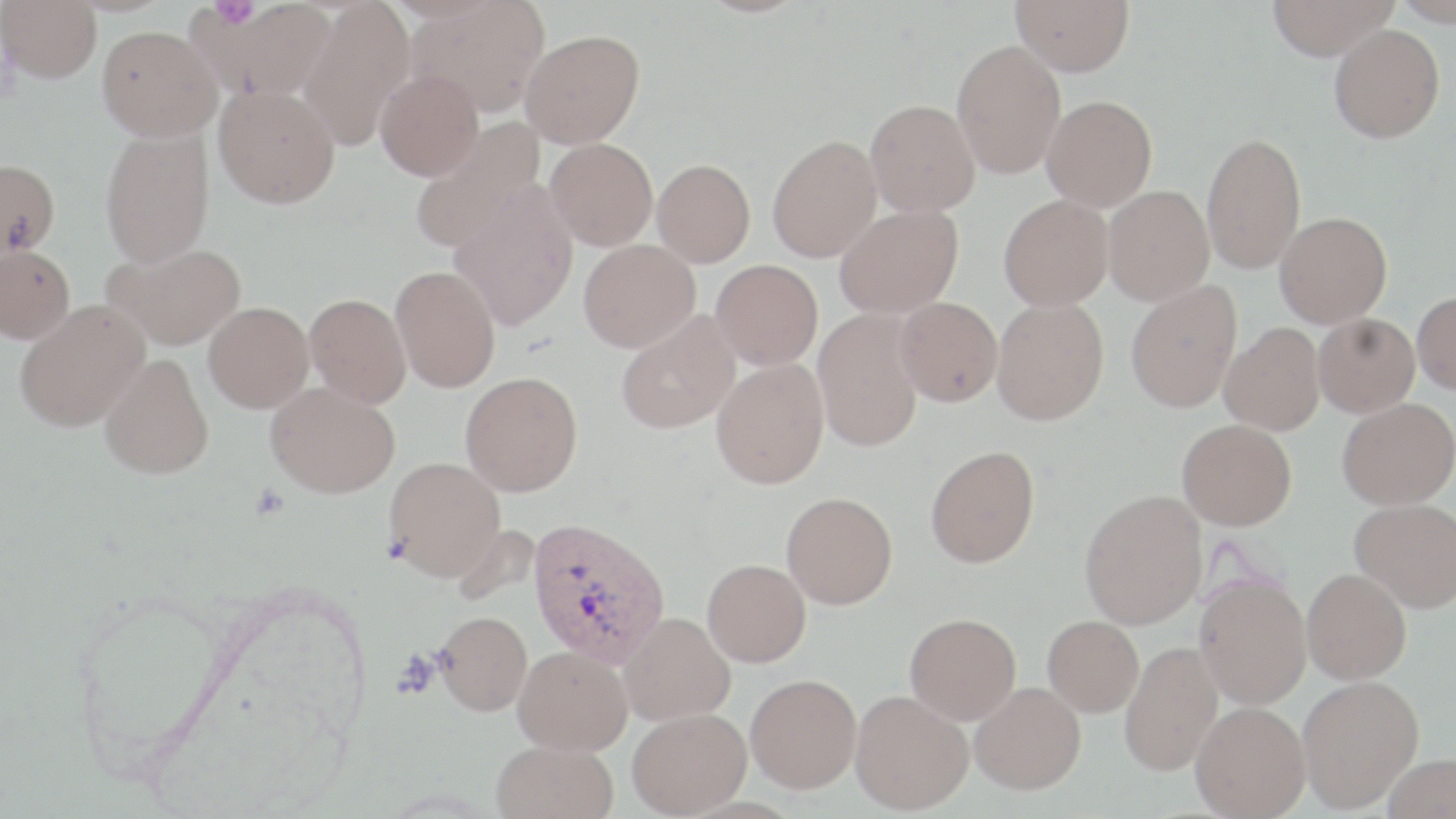
{
  "slide_level_diagnosis": "Plasmodium vivax",
  "image_size": "1456×819 pixels",
  "stain": "May-Grünwald-Giemsa",
  "modality": "optical microscopy",
  "uninfected_red_blood_cell_locations": "approximate bounding boxes as [x1, y1, x2, y2] in pixels: [1, 0, 101, 82], [200, 0, 336, 99], [407, 0, 551, 117], [1010, 0, 1134, 76], [1265, 0, 1399, 60], [1392, 0, 1456, 26], [299, 1, 417, 151], [1329, 23, 1445, 143], [97, 25, 222, 140], [520, 29, 644, 148], [952, 40, 1066, 179], [374, 69, 484, 181], [214, 85, 339, 208], [1042, 95, 1157, 211], [865, 99, 980, 216], [407, 119, 545, 253], [99, 127, 214, 268], [1201, 131, 1306, 274], [767, 134, 882, 262], [545, 138, 658, 251], [0, 159, 60, 258], [652, 159, 756, 266], [449, 184, 579, 330], [1103, 185, 1214, 305], [998, 194, 1113, 311], [834, 205, 963, 318], [1275, 211, 1392, 327], [578, 240, 700, 352], [103, 242, 247, 350], [0, 244, 75, 343], [711, 259, 823, 370], [390, 265, 501, 393], [1125, 280, 1242, 412], [1412, 292, 1456, 394], [304, 293, 412, 408], [991, 295, 1109, 425], [895, 297, 1003, 406], [14, 300, 149, 431], [204, 302, 314, 413], [812, 309, 924, 452], [616, 312, 740, 434], [1314, 312, 1420, 416], [1219, 323, 1325, 435], [100, 353, 214, 479], [711, 358, 829, 489], [459, 371, 582, 497], [266, 382, 400, 498], [1337, 397, 1456, 510], [1177, 418, 1297, 530], [925, 445, 1040, 568], [384, 456, 506, 581], [1079, 490, 1207, 629], [780, 491, 898, 609], [1351, 499, 1456, 612], [702, 559, 811, 667], [1302, 568, 1412, 684], [1195, 576, 1312, 709], [435, 611, 532, 715], [618, 612, 735, 725], [905, 612, 1021, 724], [1043, 615, 1144, 717], [1119, 641, 1224, 775], [514, 645, 633, 755], [745, 673, 861, 793], [1297, 675, 1423, 812], [970, 682, 1086, 795], [850, 689, 974, 815], [1191, 701, 1310, 818], [627, 707, 751, 818], [491, 740, 618, 819], [1383, 753, 1456, 818]",
  "field_of_view": "one of a larger specimen",
  "platelet_locations": "approximate bounding boxes as [x1, y1, x2, y2] in pixels: [211, 0, 259, 28]",
  "preparation": "thin blood smear",
  "plasmodium_vivax_infected_red_blood_cell_locations": "approximate bounding boxes as [x1, y1, x2, y2] in pixels: [526, 516, 670, 667]",
  "magnification": "1000x"
}